Assess this cell for malaria.
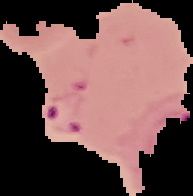
Parasitized.

Image is 193×196 pixels. From a thin blood smear. Segmented cell region on a black background.